Assess this cell for malaria.
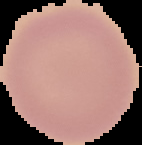

Uninfected.

Summary:
  - Image size: 142×145 pixels
  - Image type: segmented cell region on a black background
  - Preparation: thin blood film